Name the parasite shown.
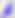

Toxoplasma gondii.

Summary:
  - Modality: photomicrograph
  - Magnification: 400x